Look for Plasmodium parasites.
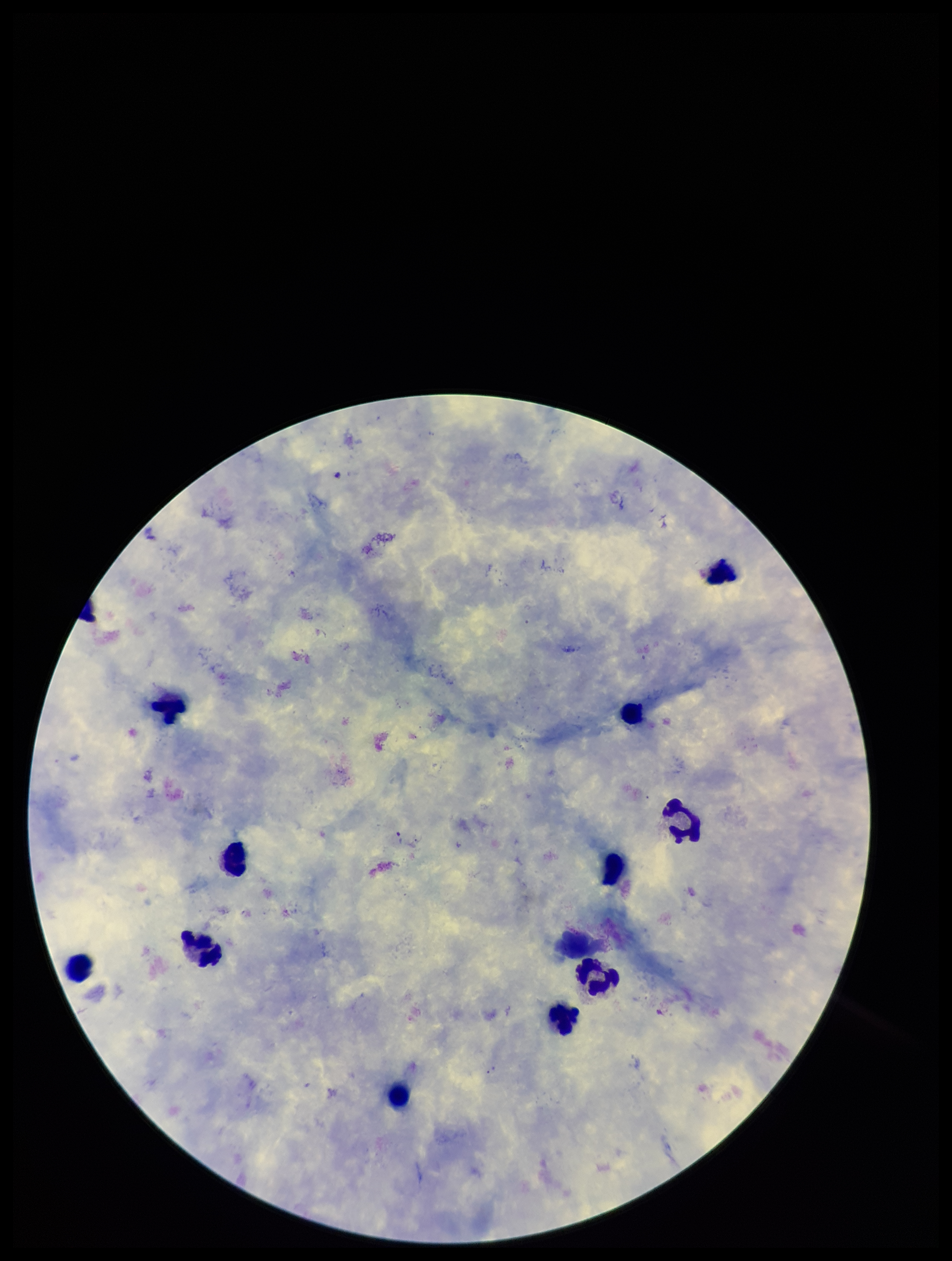

None seen.

Summary:
  - Leukocyte count: 11
  - Stain: Giemsa
  - Parasite count: 0
  - Image size: 952×1261 pixels
  - Capture: smartphone photograph through the microscope eyepiece
  - Field of view: one from this slide
  - Species reported for this patient: Plasmodium falciparum
  - Patient malaria status: positive
  - Preparation: thick